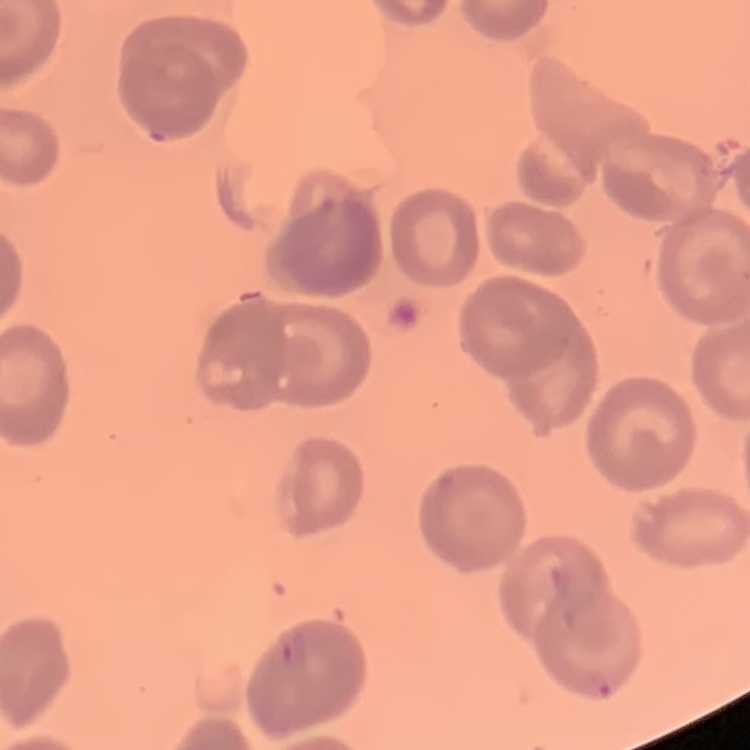

red blood cell morphology = no rouleaux formation
preparation = thin blood smear
image type = one tile cut from a larger photomicrograph
stain = Field's or Giemsa